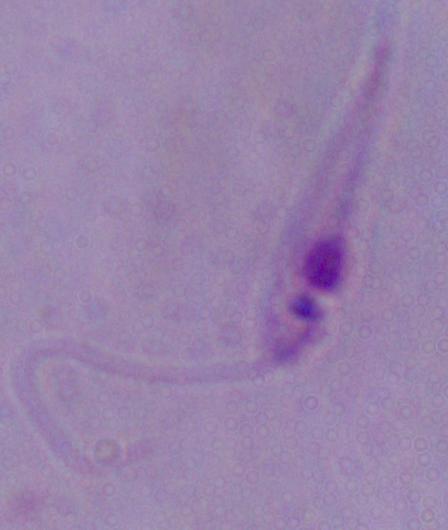

modality = photomicrograph
identification = Leishmania
magnification = 1000x